Comment on the morphology of the red blood cells.
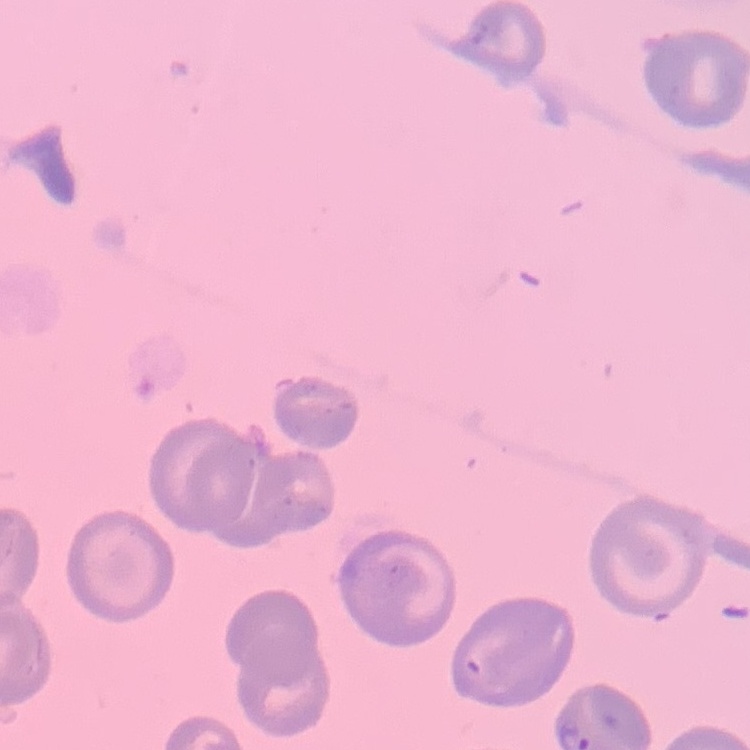

They show no rouleaux formation.

Square crop of a larger photomicrograph. Thin blood smear. Field's or Giemsa stain.